Assess this cell for malaria.
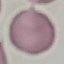
It is uninfected.

Acquired by smartphone through the microscope eyepiece. Thin blood smear. Giemsa stain. Automatically extracted cell patch, resized to 64 × 64 pixels.